Outline each blood parasite and name the species.
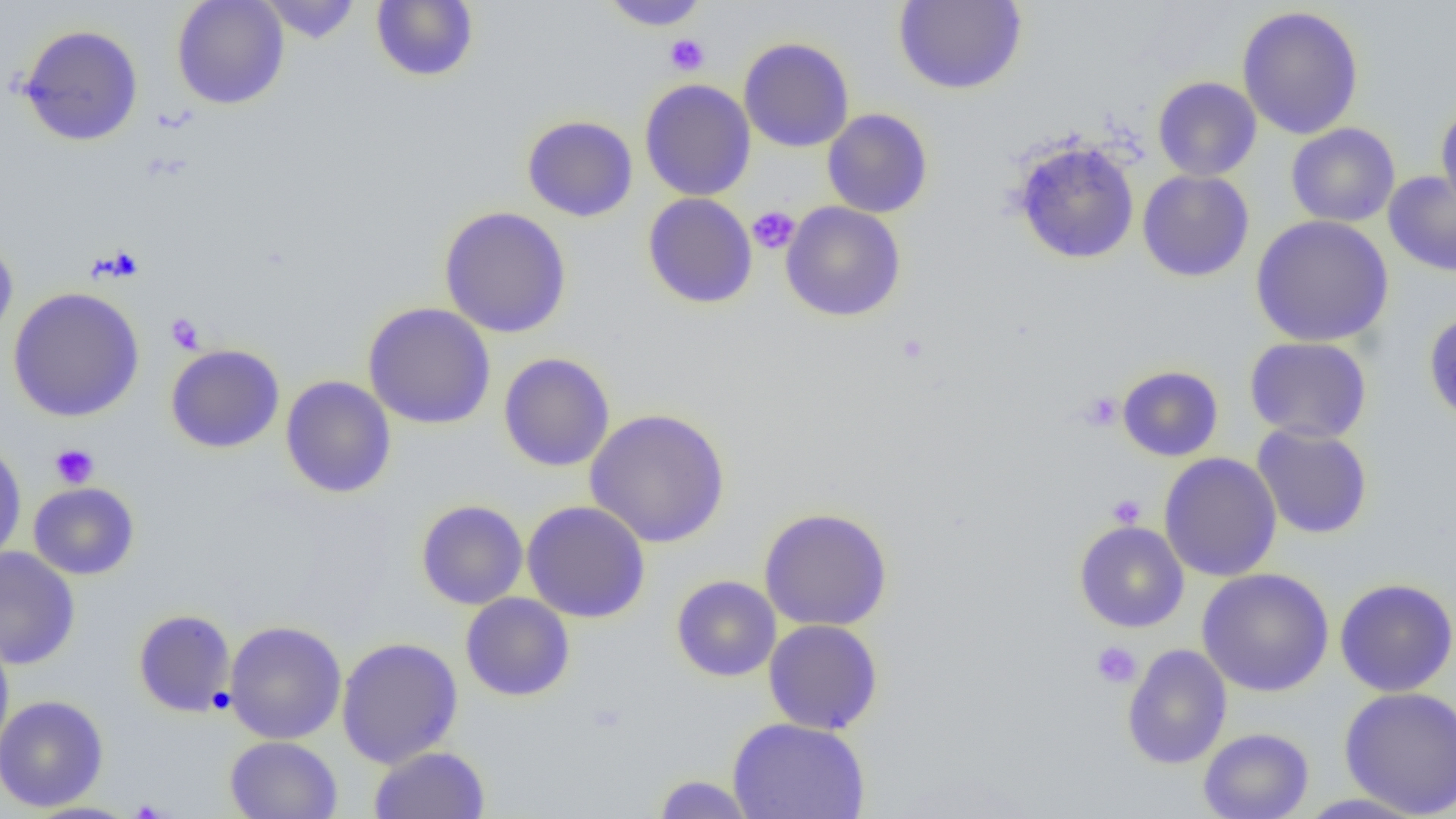

No blood parasites seen.

slide_level_diagnosis: negative for blood parasites
magnification: 1000x
modality: optical microscopy
preparation: thin blood film
image_size: 1456×819 pixels
field_of_view: one of a larger specimen
uninfected_red_blood_cell_locations: 'approximate bounding boxes as (x1, y1, x2, y2) in pixels: (171, 0, 290, 110), (259, 0, 361, 44), (893, 0, 1028, 95), (371, 1, 479, 82), (599, 1, 710, 31), (1237, 6, 1364, 139), (18, 24, 144, 146), (738, 37, 855, 153), (1152, 77, 1262, 181), (639, 78, 756, 201), (1435, 102, 1456, 216), (822, 108, 933, 218), (521, 115, 638, 222), (1286, 123, 1400, 227), (1011, 139, 1140, 265), (1137, 170, 1254, 282), (1383, 171, 1456, 277), (642, 192, 758, 308), (781, 201, 906, 322), (439, 206, 572, 338), (1250, 215, 1394, 347), (0, 237, 18, 343), (8, 287, 145, 422), (362, 302, 496, 430), (1423, 310, 1456, 427), (1244, 336, 1372, 443), (165, 344, 285, 453), (498, 352, 615, 472), (1116, 365, 1224, 462), (280, 375, 396, 498), (585, 408, 731, 548), (1252, 423, 1373, 539), (0, 442, 27, 564), (1159, 452, 1282, 582), (28, 482, 139, 579), (416, 500, 528, 609), (521, 501, 651, 623), (759, 507, 893, 631), (1074, 521, 1189, 633), (0, 546, 80, 670), (1196, 568, 1334, 696), (671, 576, 781, 682), (1334, 578, 1456, 697), (460, 592, 575, 701), (133, 609, 236, 717), (763, 618, 884, 735), (224, 620, 347, 745), (0, 633, 14, 756), (337, 636, 463, 768), (1121, 643, 1232, 770), (1339, 686, 1456, 817), (0, 694, 109, 812), (727, 717, 870, 818), (1198, 727, 1314, 819), (224, 736, 343, 818), (369, 746, 490, 819), (652, 774, 755, 818), (1291, 792, 1432, 819), (21, 801, 142, 819)'
platelet_locations: 'approximate bounding boxes as (x1, y1, x2, y2) in pixels: (665, 33, 709, 76), (747, 206, 800, 254), (166, 313, 205, 354), (896, 333, 930, 365), (1079, 392, 1122, 432), (49, 443, 99, 489), (1107, 494, 1146, 528), (1091, 641, 1141, 688)'